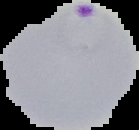
Malaria status: parasitized. Segmented cell region on a black background. From a thin blood smear. Image is 139×130 pixels.